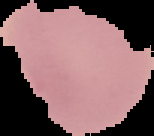

image type = cell region segmented out of the field of view; surrounding area masked to black
image size = 154×136 pixels
result = no Plasmodium parasites detected
preparation = thin blood film